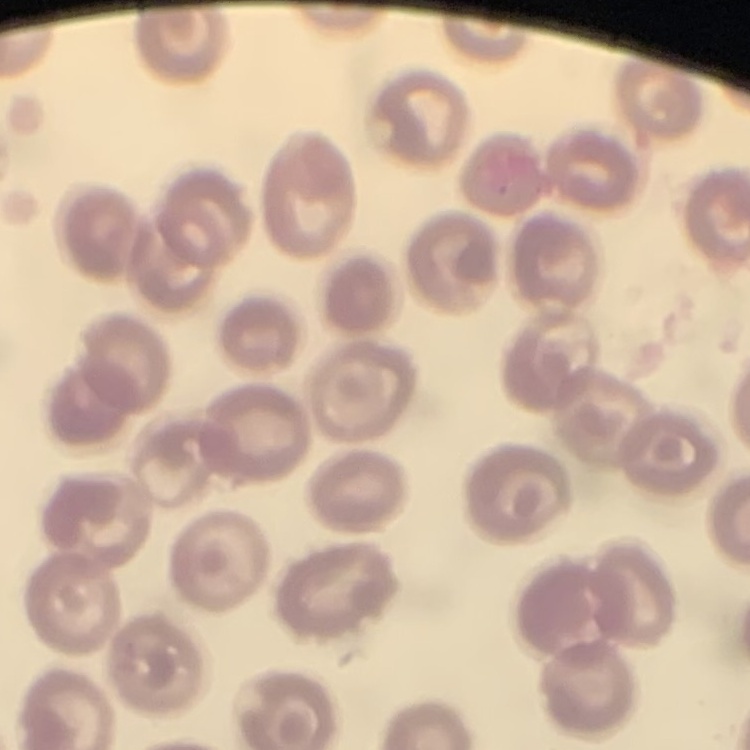

Summary:
  - Red blood cell morphology: no rouleaux formation
  - Image type: square crop of a larger photomicrograph
  - Preparation: thin blood film
  - Stain: Field's or Giemsa